Report the malaria status of this cell.
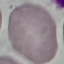
It is uninfected.

capture: smartphone camera at the microscope eyepiece
stain: Giemsa
image_type: cell patch, automatically extracted from a larger field of view and resized to 64 × 64 pixels
preparation: thin blood smear